Classify this cell by malaria status.
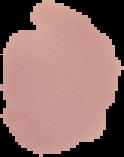

It is uninfected.

Cell region segmented out of the field of view; the surrounding area is masked to black. Image is 124×157 pixels. From a thin blood film.